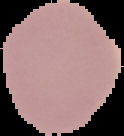
Summary:
  - Preparation: thin blood smear
  - Image size: 124×136 pixels
  - Image type: segmented cell region on a black background
  - Result: negative for malaria parasites